Point out every malaria parasite and every leukocyte.
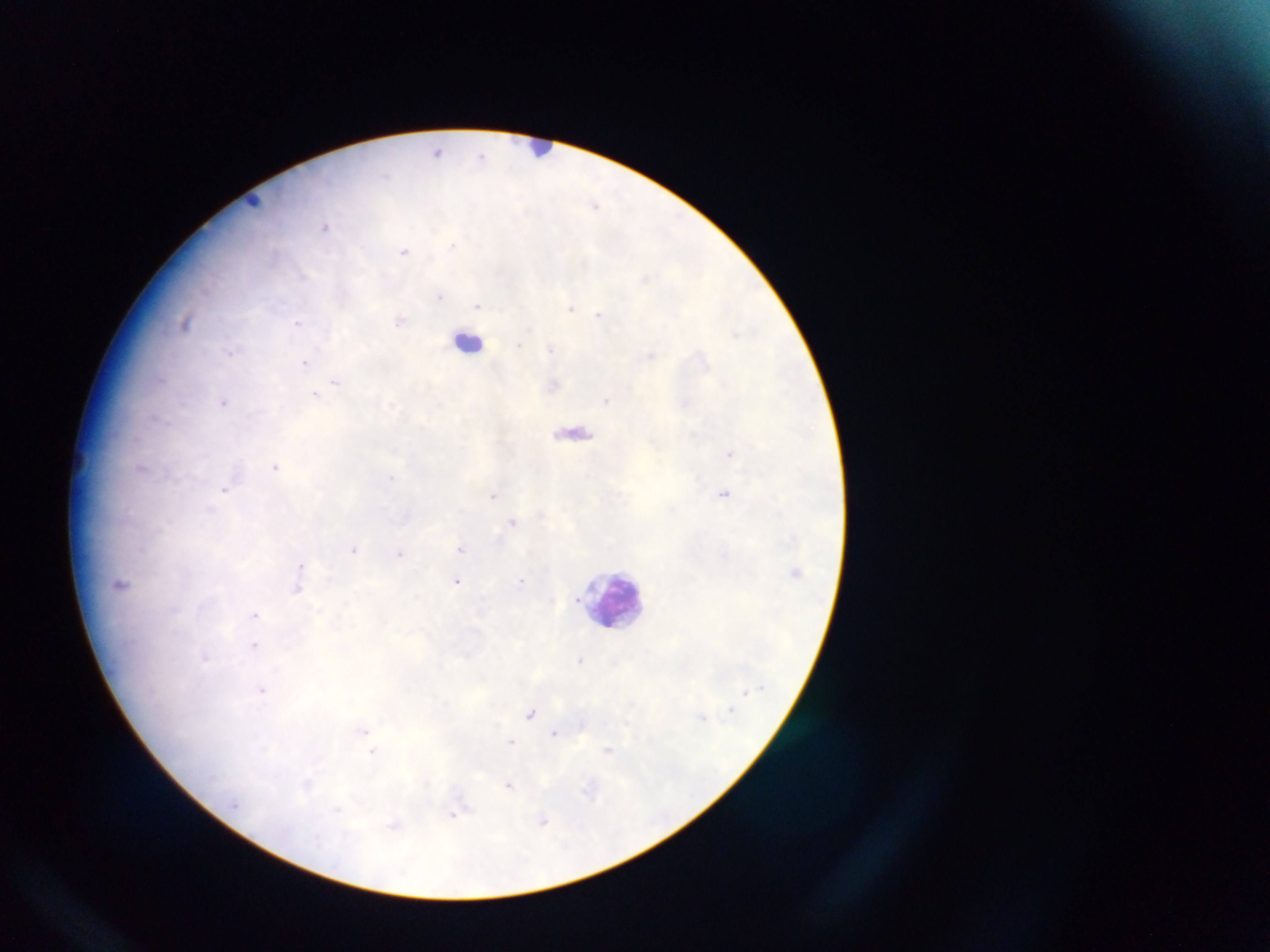

Approximate centers as (x, y) in pixels.
Malaria parasites: (481, 153), (596, 204), (326, 228), (453, 244), (404, 250), (645, 277), (439, 295), (478, 304), (570, 308), (598, 314), (298, 322), (520, 343), (551, 348), (230, 352), (305, 362), (337, 382), (314, 394), (607, 401), (224, 402), (275, 466), (393, 479), (225, 489), (493, 497), (513, 522), (355, 549), (461, 549), (401, 552), (522, 579), (457, 580), (255, 615), (255, 647), (580, 660), (262, 690), (531, 712), (363, 730), (555, 732), (511, 740), (609, 750), (508, 786), (453, 815), (545, 821).
Leukocytes: (543, 150), (468, 341), (608, 602).

Summary:
  - Capture: mobile-phone photograph through a microscope
  - Country: Ghana
  - Field of view: single
  - Image size: 1270×952 pixels
  - Preparation: thick blood smear